Report the malaria status.
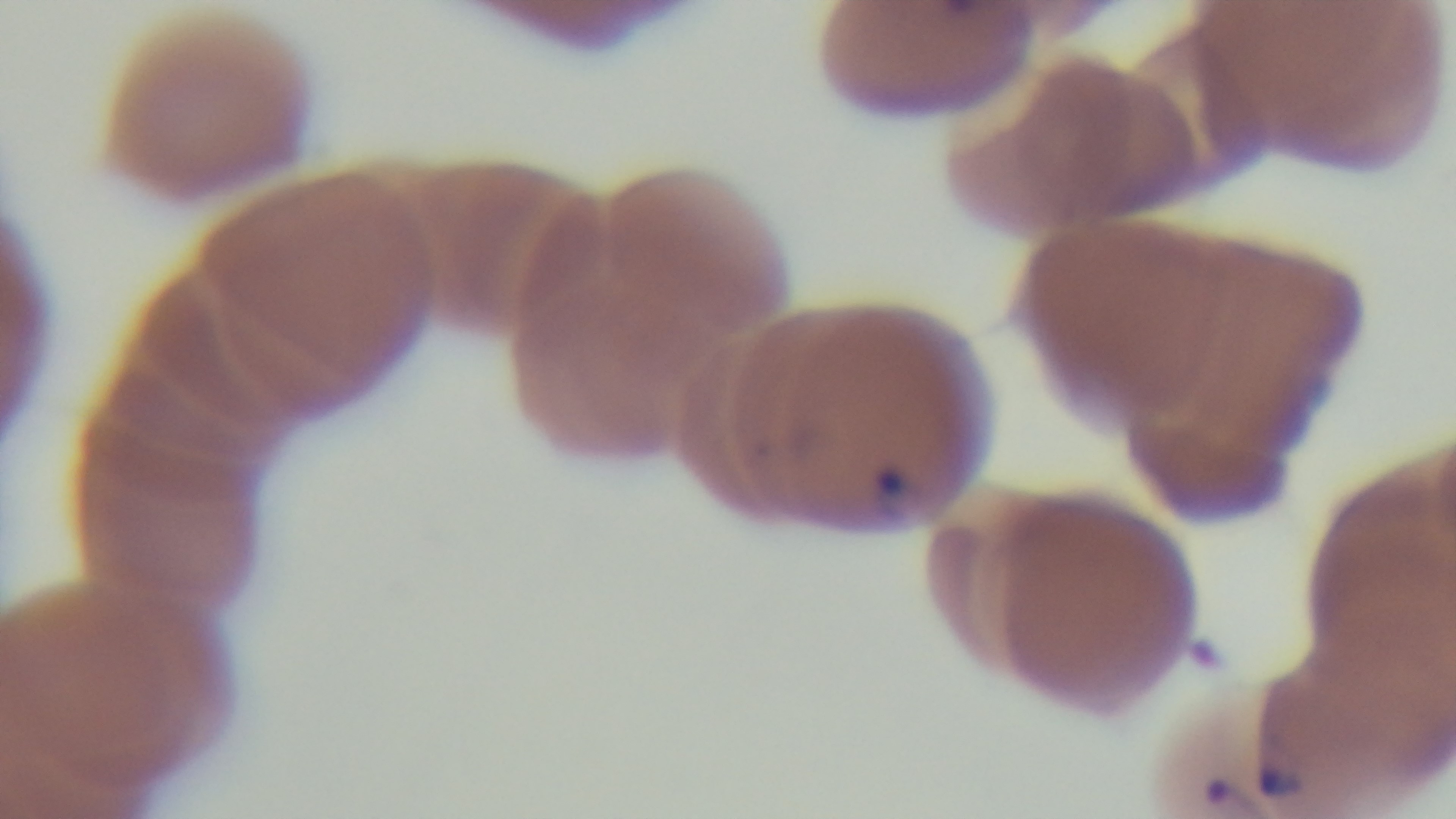
It is infected.

Captured with a mounted 4K digital camera. Light microscopy. Giemsa-stained. Preparation: thin. Oil-immersion objective, 100x. Single field of view.